Point out each Plasmodium parasite.
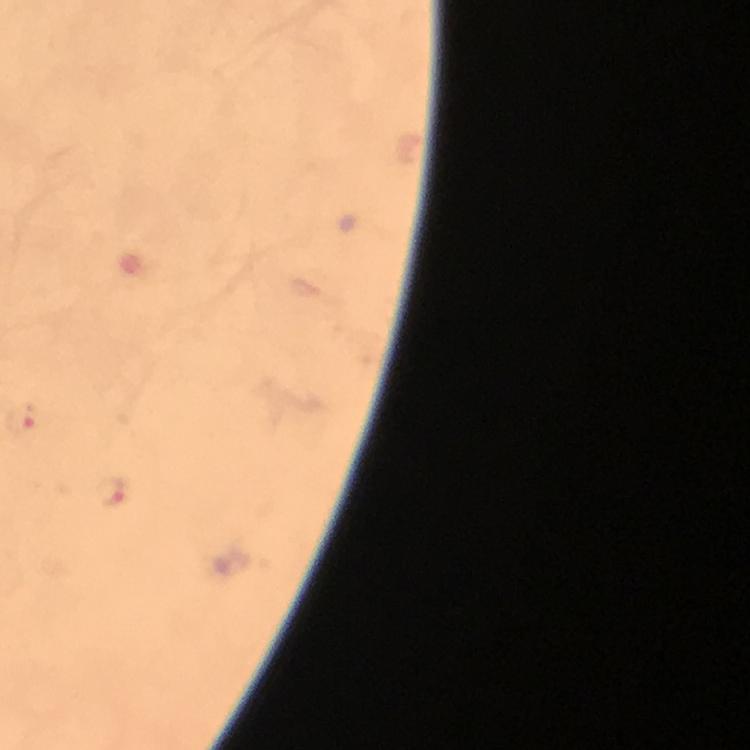

Approximate object centers, in pixels from the top-left corner.
Plasmodium parasites: (x=110, y=491).

Thick smear. Image is 750×750 pixels. Immersion oil applied. Photographed with a smartphone mounted on the microscope. From a malaria diagnostic workup. At 100x magnification. A crop from one field of view. Giemsa-stained preparation.